Assess this cell for malaria.
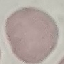
It is uninfected.

image type = cell patch, automatically extracted from a larger field of view and resized to 64 × 64 pixels
capture = smartphone through the microscope eyepiece
stain = Giemsa
preparation = thin smear